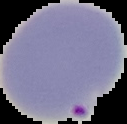
image type = segmented cell region with the area outside set to black
image size = 127×124 pixels
preparation = thin blood smear
result = Plasmodium parasites detected